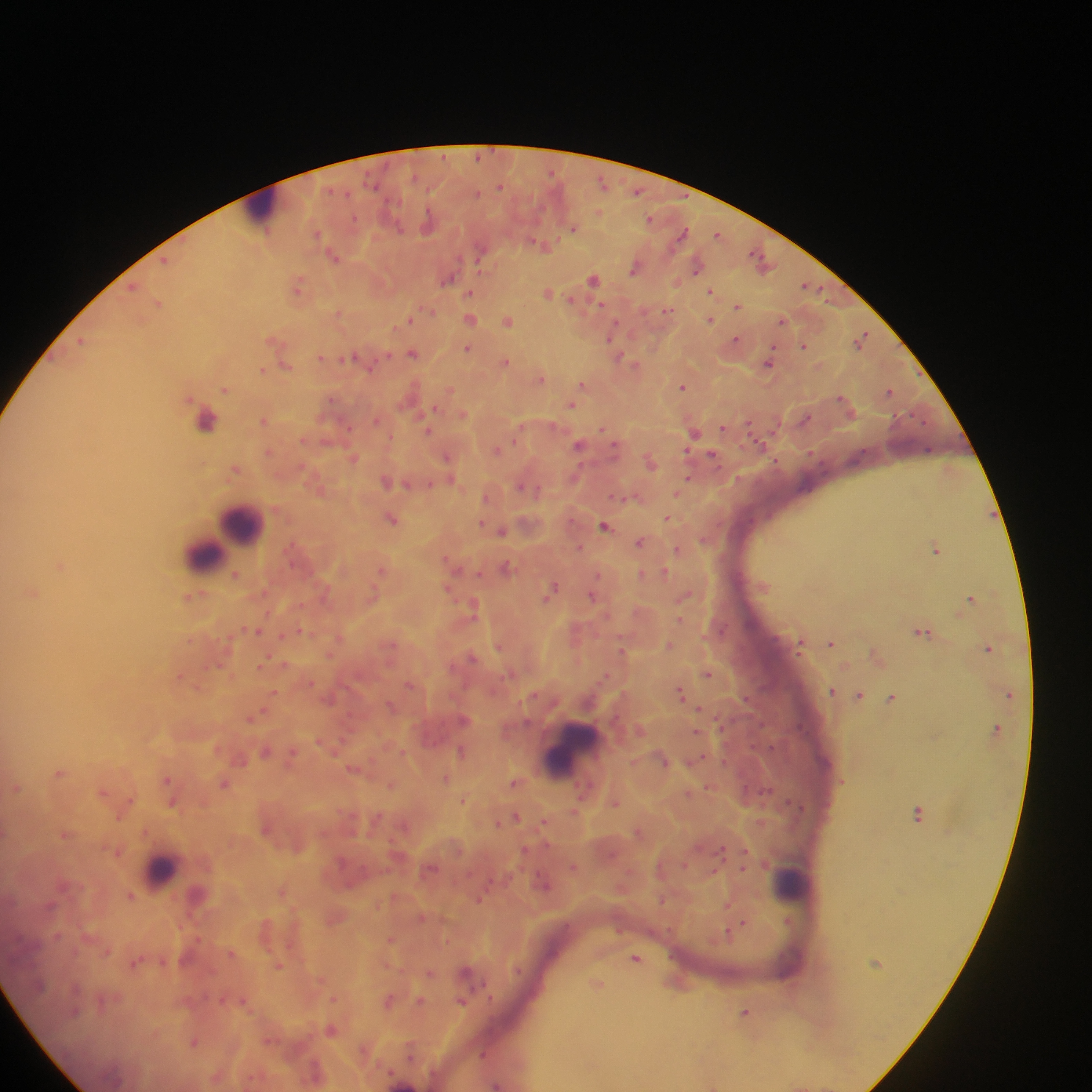

Approximate centers as (x, y) in pixels.
Summary:
  - Leukocyte locations: (264, 207), (215, 424), (243, 523), (232, 530), (202, 554), (571, 750), (160, 869), (792, 884)
  - Malaria parasite locations: (603, 182), (500, 186), (637, 191), (650, 218), (429, 221), (574, 227), (718, 233), (683, 234), (543, 245), (334, 255), (166, 259), (761, 260), (636, 266), (697, 266), (448, 277), (594, 279), (133, 285), (299, 285), (809, 287), (711, 291), (470, 292), (549, 293), (159, 303), (738, 305), (600, 306), (668, 310), (430, 311), (339, 314), (470, 318), (409, 319), (710, 319), (782, 320), (508, 321), (611, 335), (861, 338), (735, 339), (82, 340), (276, 342), (804, 345), (467, 348), (413, 353), (322, 357), (349, 358), (624, 360), (505, 361), (285, 363), (370, 363), (768, 363), (263, 370), (541, 378), (583, 384), (683, 386), (225, 389), (450, 390), (889, 391), (571, 404), (436, 407), (462, 415), (265, 419), (377, 420), (723, 427), (427, 429), (602, 429), (694, 431), (758, 442), (579, 443), (497, 449), (268, 452), (712, 455), (449, 457), (353, 458), (777, 461), (650, 462), (236, 468), (688, 479), (387, 481), (408, 484), (430, 484), (524, 486), (679, 493), (487, 496), (632, 498), (392, 518), (666, 518), (481, 523), (605, 525), (501, 531), (704, 539), (641, 541), (580, 547), (678, 549), (937, 549), (447, 559), (61, 566), (506, 567), (382, 568), (664, 572), (236, 574), (641, 574), (448, 589), (325, 590), (552, 590), (33, 592), (687, 594), (373, 595), (593, 595), (195, 597), (972, 597), (474, 605), (681, 620), (257, 630), (301, 631), (924, 631), (283, 635), (339, 637), (801, 642), (831, 643), (669, 645), (499, 646), (988, 647), (623, 651), (330, 654), (877, 655), (472, 657), (285, 664), (263, 665), (708, 673), (181, 675), (310, 682), (411, 684), (832, 691), (681, 692), (274, 693), (1009, 693), (860, 694), (892, 697), (700, 707), (262, 711), (250, 718), (997, 728), (697, 732), (266, 750), (462, 751), (403, 752), (293, 755), (241, 759), (664, 759), (698, 759), (354, 768), (60, 772), (445, 778), (168, 779), (516, 782), (225, 783), (391, 784), (15, 787), (709, 788), (103, 791), (689, 794), (463, 800), (616, 802), (173, 803), (574, 811), (919, 813), (516, 816), (499, 822), (545, 822), (405, 825), (639, 831), (66, 833), (745, 850), (118, 852), (684, 864), (573, 867), (430, 869), (742, 869), (713, 871), (544, 884), (282, 890), (131, 896), (479, 899), (728, 902), (422, 917), (788, 921), (743, 923), (735, 929), (729, 932), (391, 938), (107, 950), (231, 952), (636, 958), (135, 962), (279, 965), (430, 972), (597, 983), (334, 998), (421, 1000), (244, 1001), (389, 1001), (462, 1001), (747, 1013), (331, 1029), (195, 1042), (365, 1050), (413, 1051), (484, 1053), (316, 1073), (217, 1075), (496, 1084), (712, 1085)
  - Capture: mobile-phone photograph through a microscope
  - Image size: 1092×1092 pixels
  - Field of view: single
  - Country: Ghana
  - Preparation: thick blood smear